Report the malaria status of this cell.
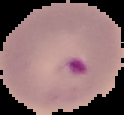
Parasitized.

image size = 124×115 pixels
image type = cell region segmented out of the field of view; surrounding area masked to black
preparation = thin blood film